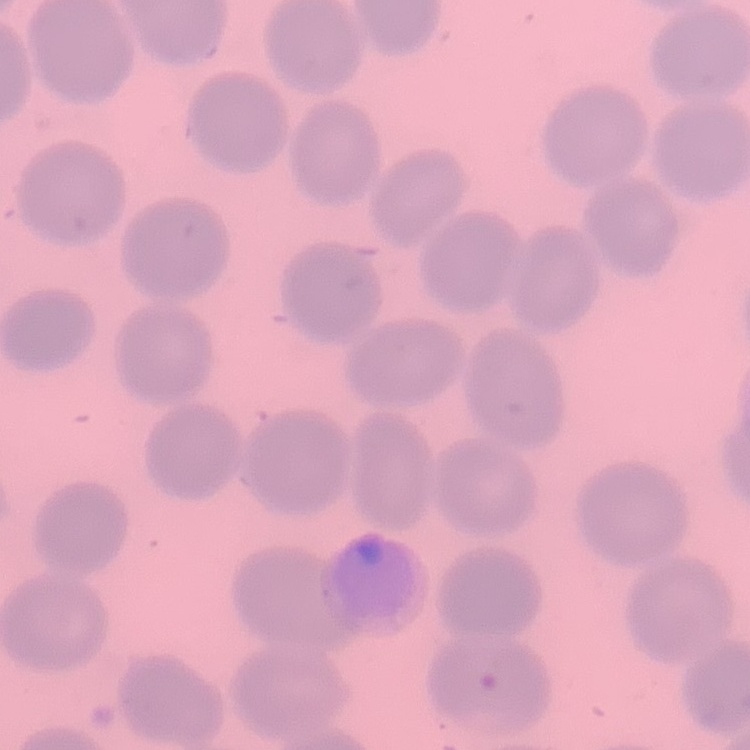

Summary:
  - Erythrocyte morphology: no rouleaux formation
  - Image type: one tile cut from a larger photomicrograph
  - Stain: Field's or Giemsa
  - Preparation: thin blood film